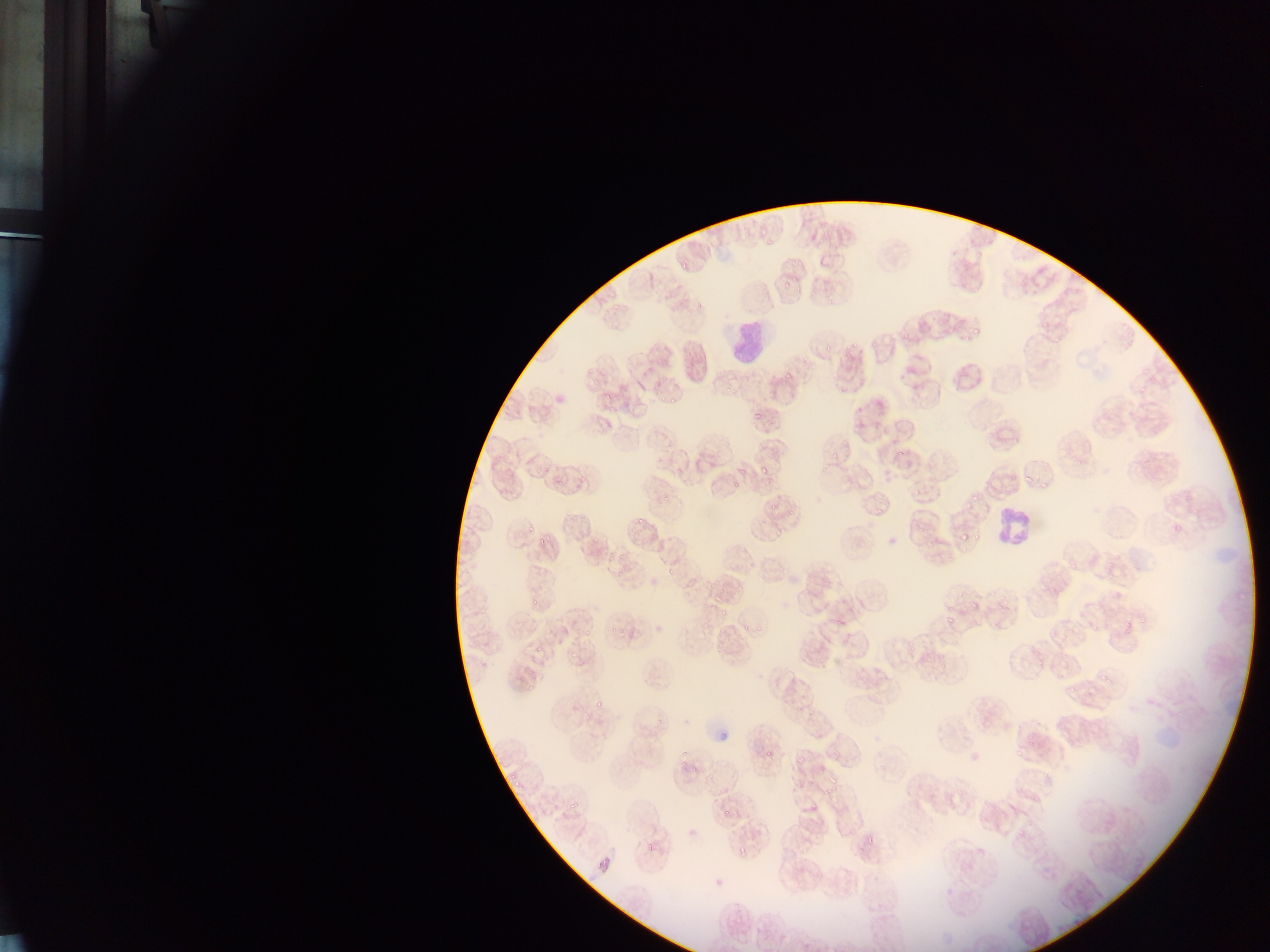

Approximate bounding boxes as left top right bottom in pixels. Leukocyte locations: 726 315 777 369; 989 500 1038 554. Malaria parasite locations: 765 235 778 247; 677 258 688 273; 782 279 795 289; 969 322 987 338; 821 339 842 350; 839 346 863 364; 785 368 796 382; 602 390 616 400; 746 408 762 422; 821 443 843 460; 891 452 909 465; 539 462 554 473; 754 463 772 480; 738 464 746 477; 504 467 514 473; 1020 472 1036 488; 1005 474 1019 487; 1039 474 1053 488; 547 480 565 490; 730 481 741 488; 965 486 986 505; 659 493 675 503; 910 494 923 498; 766 503 780 515; 869 507 890 519; 633 515 647 526; 755 520 767 532; 537 524 550 546; 1170 525 1185 535; 525 526 534 536; 770 527 784 541; 953 530 972 546; 616 552 631 563; 604 554 616 566; 664 565 677 579; 714 578 726 592; 973 590 983 612; 526 594 544 605; 710 596 724 606; 942 606 956 633; 717 610 728 620; 755 615 769 637; 832 615 846 625; 622 622 642 646; 583 626 591 636; 741 626 751 636; 728 630 739 637; 711 640 723 654; 535 643 543 651; 1030 649 1050 664; 565 650 578 661; 728 656 739 669; 1099 677 1111 685; 523 681 536 694; 1063 682 1077 699; 592 698 608 708; 761 742 783 758; 675 750 685 772; 791 754 813 768; 689 764 701 778; 511 766 527 789; 828 773 836 789; 796 778 819 796; 707 795 720 807; 723 803 733 823; 841 823 858 842; 861 834 879 851; 645 842 659 858; 732 846 750 859; 715 875 725 885. Single field of view. Thin blood film. Sample from Ghana. Image is 1270×952 pixels. Photographed through a microscope with a mobile-phone camera.